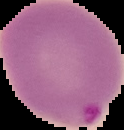
{
  "image_type": "segmented cell region with the area outside set to black",
  "result": "malaria parasites identified",
  "image_size": "124×130 pixels",
  "preparation": "thin blood film"
}